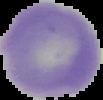

image type = segmented cell region with the area outside set to black
preparation = thin blood film
image size = 103×100 pixels
result = negative for malaria parasites